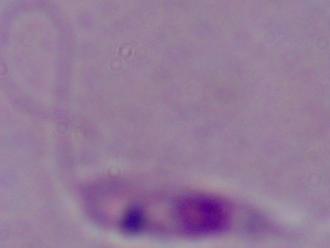

Summary:
  - Magnification: 1000x
  - Modality: micrograph
  - Identification: Leishmania